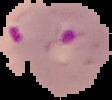
From a thin blood smear. The area outside the segmented cell region is set to black. Malaria status: parasitized. Image is 112×100 pixels.